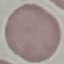 Result: no malaria parasites detected. Thin blood film. Giemsa-stained preparation. Acquired by smartphone through the microscope eyepiece. Automatically extracted cell patch, resized to 64 × 64 pixels.